Comment on the morphology of the red blood cells.
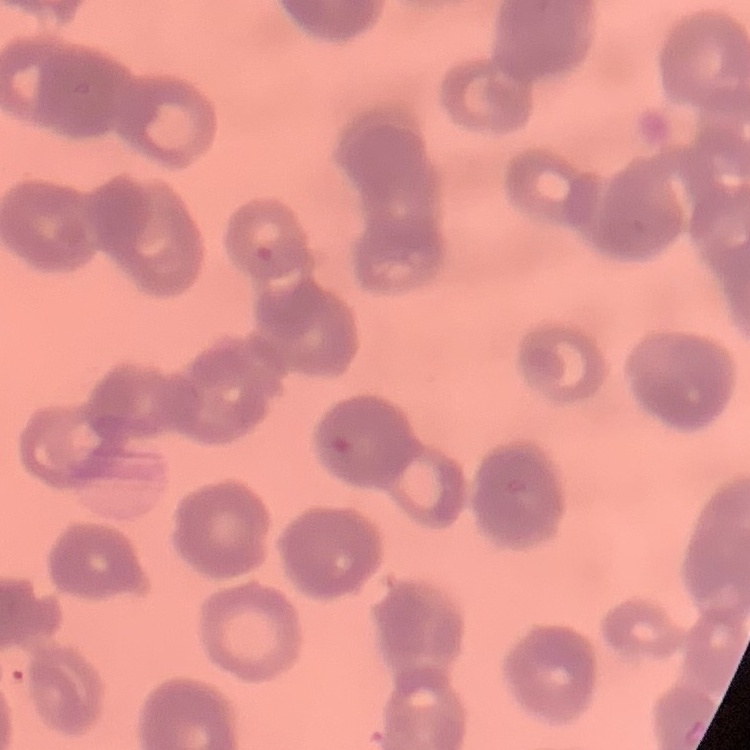
Rouleaux formation.

Thin blood smear. Stained with either Field's or Giemsa. Square crop of a larger photomicrograph.